Identify the cell.
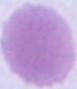

An erythrocyte.

modality = micrograph
magnification = 1000x